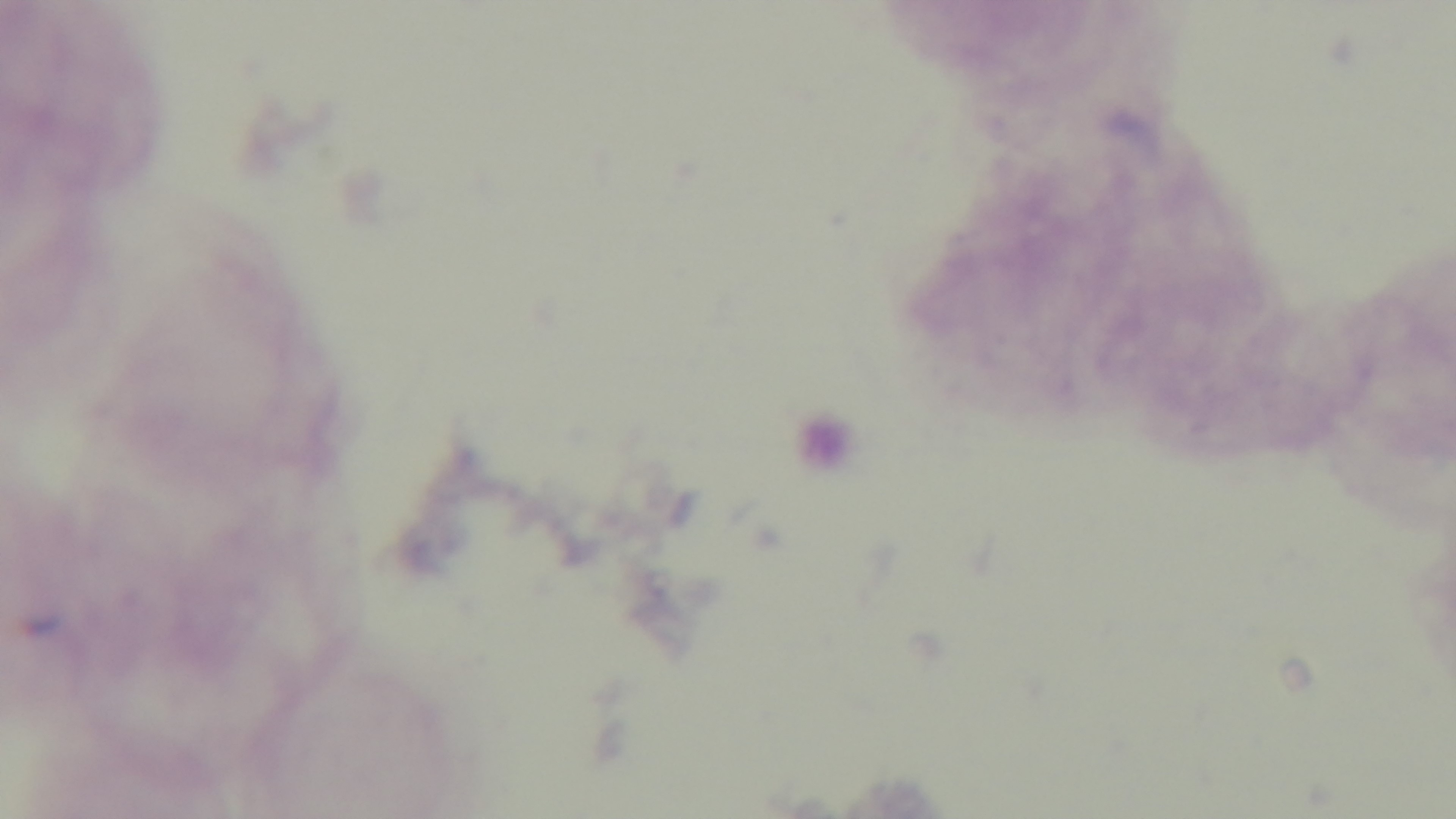

Light microscopy. Preparation: thick smear. Giemsa-stained. Mounted 4K digital camera. Single field of view. Malaria status: uninfected. Oil-immersion objective, 100x.